Assess this cell for malaria.
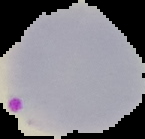

It is parasitized.

{
  "image_type": "cell region segmented out of the field of view; surrounding area masked to black",
  "image_size": "145×139 pixels",
  "preparation": "thin blood film"
}